Name the parasite shown.
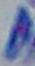

Toxoplasma gondii.

modality: micrograph
magnification: 1000x